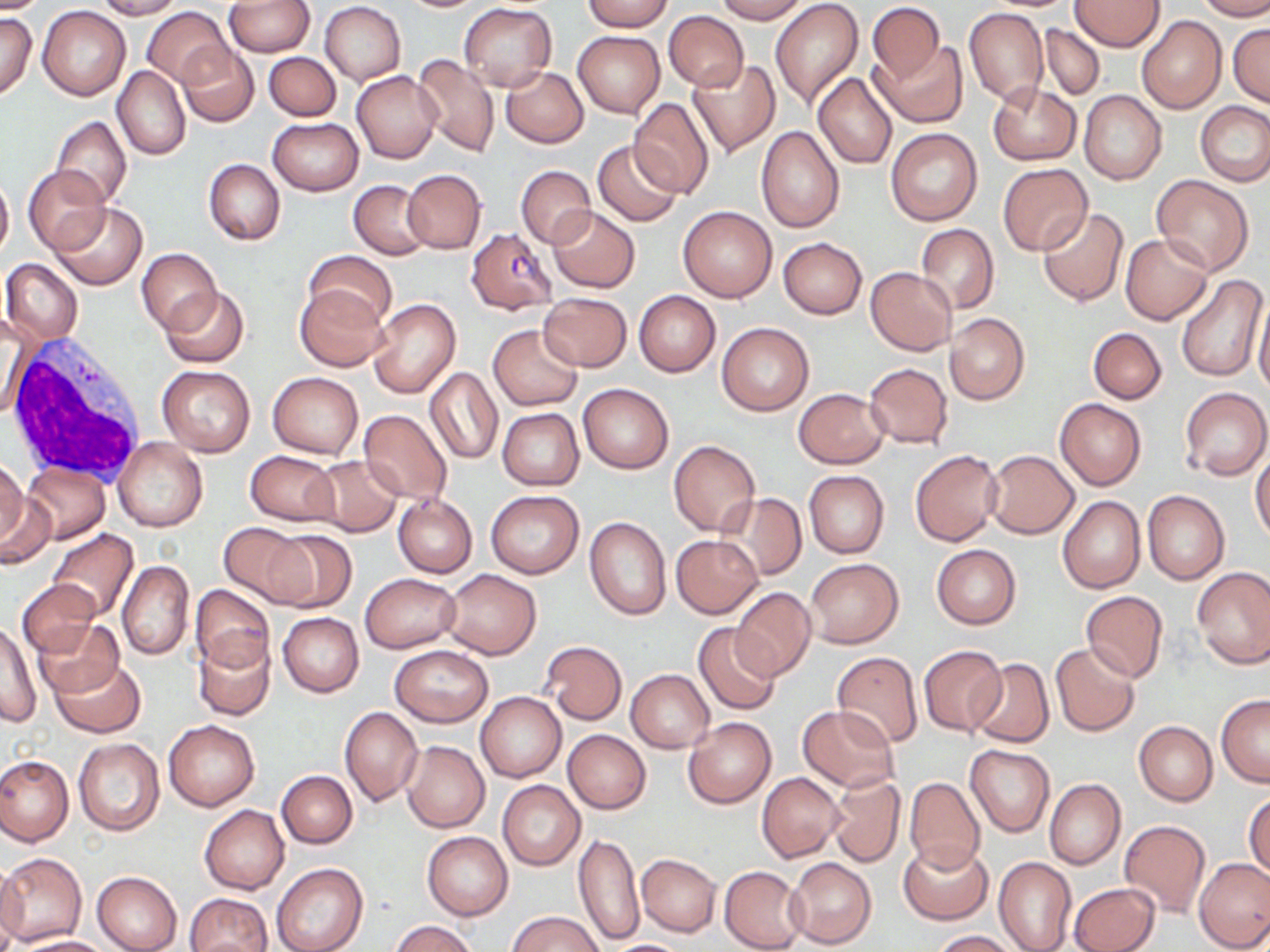
Approximate bounding boxes as named x1/y1/x2/y2 corners in pixels. Plasmodium falciparum-infected red blood cell locations: (x1=466, y1=228, x2=558, y2=313). White blood cell locations: (x1=4, y1=339, x2=148, y2=483). Uninfected red blood cell locations: (x1=0, y1=0, x2=52, y2=13), (x1=93, y1=0, x2=181, y2=20), (x1=582, y1=0, x2=671, y2=31), (x1=715, y1=0, x2=807, y2=23), (x1=770, y1=0, x2=864, y2=111), (x1=1198, y1=0, x2=1270, y2=21), (x1=224, y1=1, x2=315, y2=57), (x1=1072, y1=1, x2=1165, y2=51), (x1=319, y1=2, x2=406, y2=85), (x1=459, y1=3, x2=557, y2=90), (x1=867, y1=3, x2=943, y2=83), (x1=38, y1=6, x2=130, y2=100), (x1=143, y1=7, x2=231, y2=86), (x1=963, y1=7, x2=1048, y2=105), (x1=1035, y1=8, x2=1150, y2=83), (x1=1, y1=11, x2=37, y2=100), (x1=663, y1=11, x2=749, y2=91), (x1=1136, y1=16, x2=1226, y2=116), (x1=1228, y1=22, x2=1270, y2=107), (x1=1038, y1=24, x2=1105, y2=100), (x1=573, y1=30, x2=665, y2=119), (x1=871, y1=41, x2=967, y2=129), (x1=176, y1=42, x2=259, y2=127), (x1=264, y1=52, x2=341, y2=120), (x1=412, y1=54, x2=500, y2=158), (x1=689, y1=59, x2=779, y2=156), (x1=112, y1=66, x2=191, y2=161), (x1=501, y1=67, x2=588, y2=147), (x1=352, y1=71, x2=443, y2=163), (x1=812, y1=72, x2=897, y2=169), (x1=989, y1=82, x2=1081, y2=165), (x1=1079, y1=90, x2=1167, y2=184), (x1=629, y1=98, x2=714, y2=198), (x1=1196, y1=102, x2=1270, y2=186), (x1=51, y1=116, x2=131, y2=208), (x1=268, y1=117, x2=362, y2=195), (x1=39, y1=124, x2=124, y2=285), (x1=756, y1=127, x2=844, y2=232), (x1=884, y1=128, x2=982, y2=225), (x1=592, y1=140, x2=684, y2=228), (x1=203, y1=158, x2=285, y2=245), (x1=997, y1=164, x2=1092, y2=256), (x1=24, y1=165, x2=110, y2=254), (x1=516, y1=165, x2=596, y2=248), (x1=403, y1=169, x2=486, y2=253), (x1=0, y1=172, x2=13, y2=259), (x1=1151, y1=175, x2=1254, y2=276), (x1=348, y1=180, x2=432, y2=259), (x1=49, y1=202, x2=148, y2=291), (x1=677, y1=205, x2=777, y2=302), (x1=547, y1=206, x2=640, y2=293), (x1=1036, y1=206, x2=1128, y2=307), (x1=916, y1=224, x2=998, y2=313), (x1=1120, y1=235, x2=1213, y2=325), (x1=777, y1=238, x2=866, y2=319), (x1=137, y1=248, x2=222, y2=335), (x1=305, y1=250, x2=396, y2=329), (x1=3, y1=258, x2=82, y2=346), (x1=865, y1=267, x2=957, y2=355), (x1=1175, y1=273, x2=1267, y2=382), (x1=158, y1=286, x2=250, y2=369), (x1=295, y1=287, x2=390, y2=372), (x1=1252, y1=288, x2=1270, y2=397), (x1=634, y1=291, x2=720, y2=377), (x1=538, y1=293, x2=632, y2=372), (x1=368, y1=299, x2=461, y2=398), (x1=945, y1=313, x2=1029, y2=405), (x1=2, y1=317, x2=31, y2=421), (x1=716, y1=323, x2=813, y2=416), (x1=488, y1=325, x2=583, y2=411), (x1=1088, y1=327, x2=1166, y2=404), (x1=864, y1=363, x2=953, y2=449), (x1=156, y1=365, x2=256, y2=457), (x1=425, y1=368, x2=503, y2=464), (x1=268, y1=371, x2=363, y2=459), (x1=577, y1=383, x2=674, y2=474), (x1=1180, y1=386, x2=1270, y2=480), (x1=794, y1=388, x2=889, y2=469), (x1=1055, y1=398, x2=1146, y2=491), (x1=499, y1=408, x2=583, y2=490), (x1=358, y1=409, x2=452, y2=506), (x1=115, y1=437, x2=206, y2=532), (x1=669, y1=439, x2=760, y2=534), (x1=245, y1=450, x2=340, y2=526), (x1=910, y1=450, x2=1004, y2=546), (x1=985, y1=450, x2=1079, y2=538), (x1=1251, y1=452, x2=1270, y2=542), (x1=308, y1=455, x2=402, y2=537), (x1=0, y1=458, x2=27, y2=546), (x1=24, y1=463, x2=110, y2=544), (x1=804, y1=470, x2=889, y2=558), (x1=0, y1=490, x2=57, y2=570), (x1=486, y1=490, x2=584, y2=578), (x1=1142, y1=491, x2=1229, y2=584), (x1=716, y1=493, x2=807, y2=582), (x1=393, y1=494, x2=477, y2=578), (x1=1057, y1=495, x2=1145, y2=593), (x1=584, y1=516, x2=671, y2=619), (x1=218, y1=521, x2=313, y2=607), (x1=264, y1=528, x2=356, y2=612), (x1=47, y1=530, x2=137, y2=623), (x1=671, y1=534, x2=763, y2=617), (x1=931, y1=544, x2=1021, y2=629), (x1=804, y1=558, x2=903, y2=648), (x1=117, y1=560, x2=194, y2=661), (x1=1192, y1=566, x2=1270, y2=668), (x1=440, y1=569, x2=541, y2=659), (x1=360, y1=573, x2=460, y2=653), (x1=18, y1=580, x2=100, y2=657), (x1=190, y1=584, x2=274, y2=674), (x1=730, y1=587, x2=816, y2=681), (x1=1081, y1=590, x2=1167, y2=681), (x1=278, y1=612, x2=364, y2=697), (x1=1, y1=619, x2=41, y2=728), (x1=36, y1=619, x2=125, y2=698), (x1=693, y1=623, x2=782, y2=715), (x1=193, y1=635, x2=276, y2=722), (x1=540, y1=640, x2=627, y2=725), (x1=1050, y1=642, x2=1142, y2=736), (x1=918, y1=645, x2=1007, y2=736), (x1=389, y1=646, x2=492, y2=727), (x1=832, y1=652, x2=923, y2=747), (x1=51, y1=658, x2=145, y2=737), (x1=967, y1=659, x2=1054, y2=748), (x1=626, y1=670, x2=714, y2=752), (x1=475, y1=691, x2=566, y2=781), (x1=1216, y1=695, x2=1270, y2=785), (x1=797, y1=704, x2=898, y2=792), (x1=340, y1=707, x2=423, y2=807), (x1=163, y1=719, x2=259, y2=811), (x1=683, y1=719, x2=776, y2=808), (x1=1134, y1=721, x2=1217, y2=805), (x1=563, y1=729, x2=650, y2=814), (x1=72, y1=738, x2=165, y2=836), (x1=402, y1=741, x2=490, y2=833), (x1=966, y1=746, x2=1054, y2=835), (x1=0, y1=754, x2=73, y2=847), (x1=277, y1=769, x2=357, y2=848), (x1=757, y1=772, x2=844, y2=861), (x1=827, y1=776, x2=905, y2=868), (x1=905, y1=777, x2=985, y2=872), (x1=1044, y1=779, x2=1126, y2=869), (x1=497, y1=780, x2=584, y2=870), (x1=1245, y1=791, x2=1269, y2=878), (x1=199, y1=805, x2=289, y2=894), (x1=1119, y1=819, x2=1210, y2=917), (x1=422, y1=831, x2=513, y2=920), (x1=573, y1=833, x2=643, y2=946), (x1=899, y1=841, x2=993, y2=924), (x1=0, y1=851, x2=88, y2=947), (x1=636, y1=854, x2=720, y2=935), (x1=993, y1=856, x2=1077, y2=952), (x1=1194, y1=857, x2=1270, y2=952), (x1=786, y1=858, x2=876, y2=949), (x1=0, y1=862, x2=27, y2=952), (x1=272, y1=863, x2=368, y2=952), (x1=719, y1=866, x2=806, y2=951), (x1=91, y1=871, x2=182, y2=952), (x1=1070, y1=882, x2=1159, y2=952), (x1=184, y1=893, x2=272, y2=952), (x1=507, y1=910, x2=605, y2=952), (x1=390, y1=919, x2=477, y2=952), (x1=930, y1=930, x2=1020, y2=951), (x1=15, y1=936, x2=115, y2=952), (x1=605, y1=939, x2=692, y2=952). Slide-level diagnosis: Plasmodium falciparum. 1000x magnification. Image is 1270×952 pixels. Light microscopy. One field of a larger specimen. Thin blood smear. May-Grünwald-Giemsa-stained preparation.